Assess the morphology of the red blood cells.
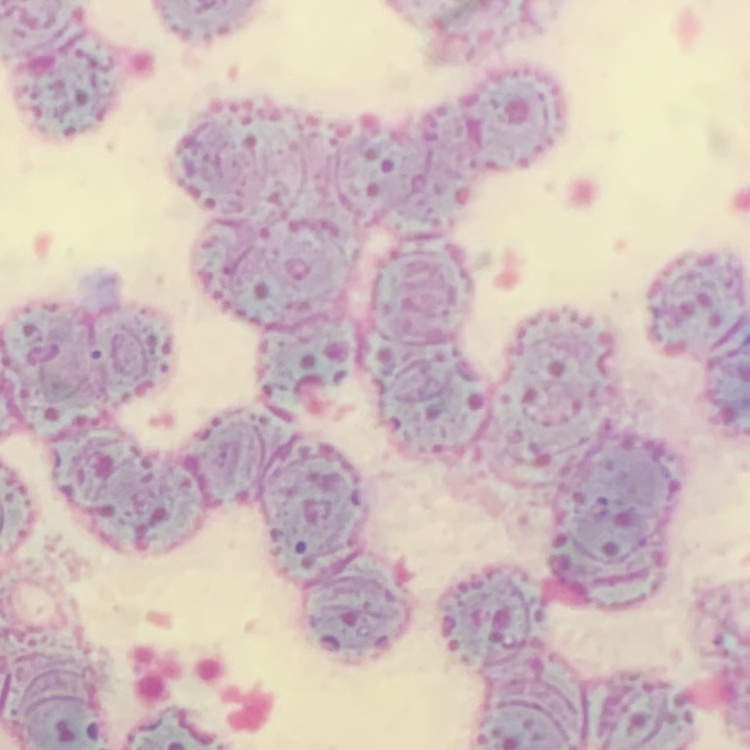

Rouleaux formation.

preparation = thin peripheral smear
image type = square crop of a larger photomicrograph
stain = Field's or Giemsa